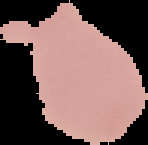

preparation: thin blood smear
result: negative for Plasmodium parasites
image_size: 148×145 pixels
image_type: segmented cell region on a black background